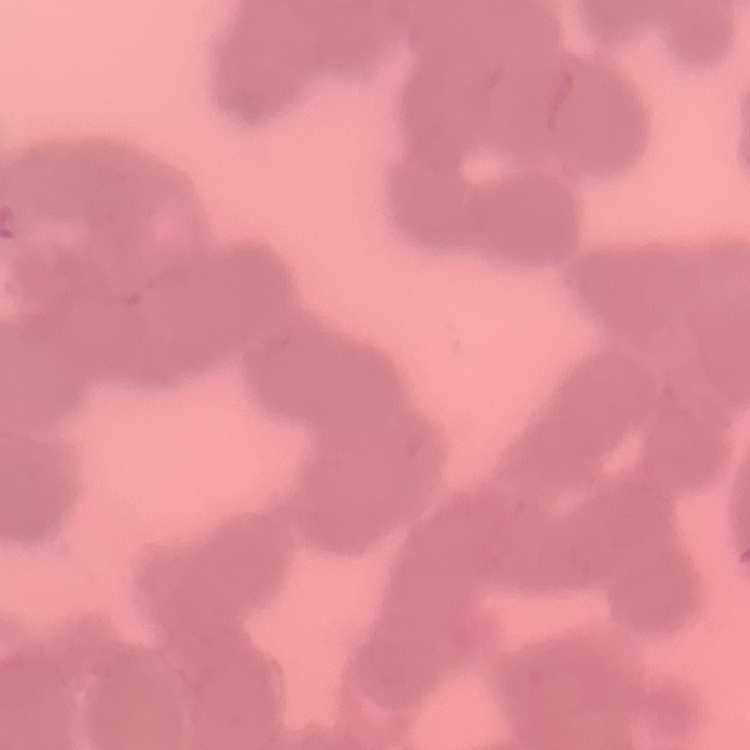
The red blood cells exhibit rouleaux formation. Stained with either Field's or Giemsa. One tile cut from a larger photomicrograph. Thin peripheral smear.